Locate and identify every blood parasite.
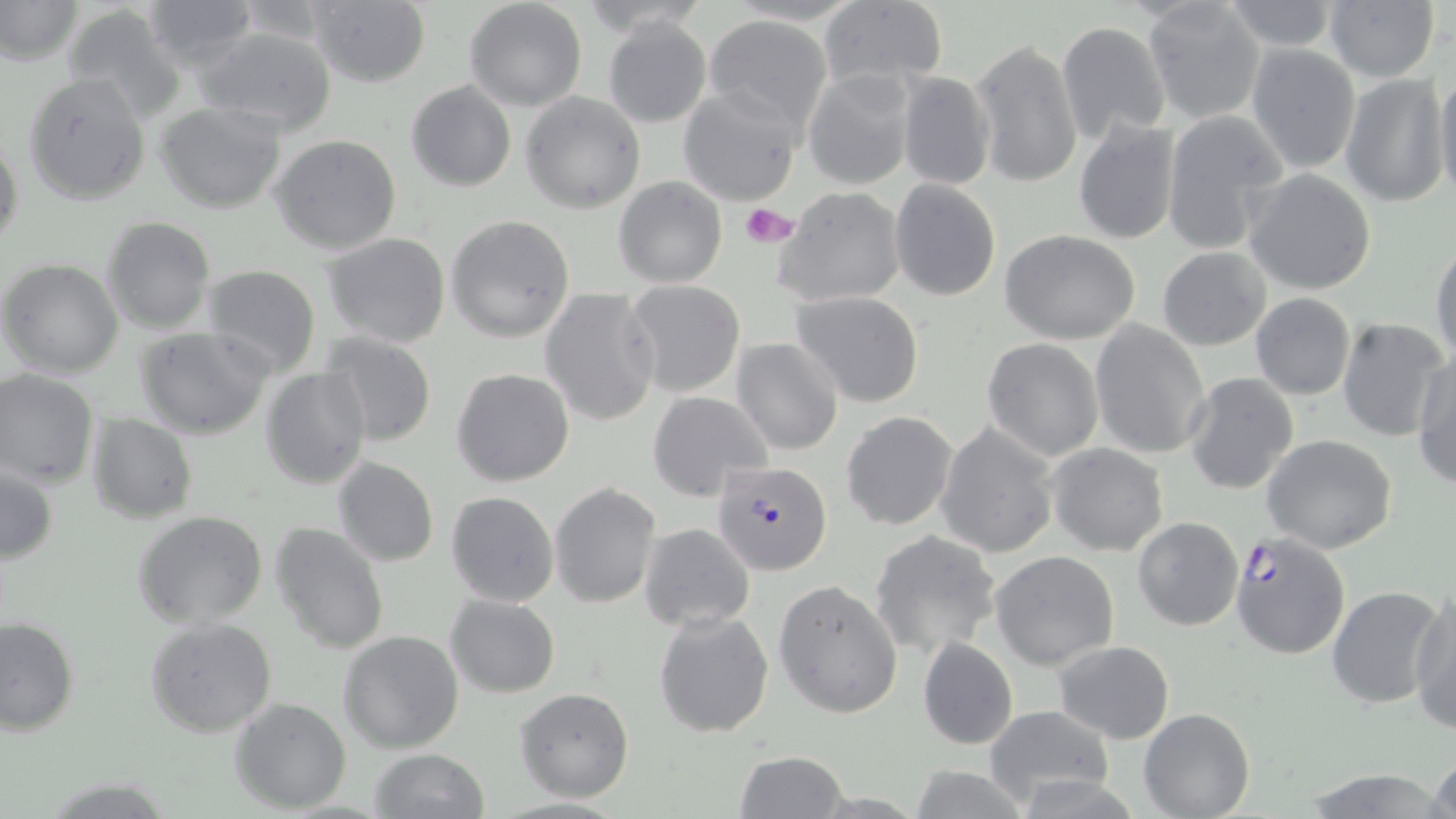
Approximate bounding boxes as [x1, y1, x2, y2] in pixels.
Plasmodium falciparum-infected red blood cells: [712, 458, 830, 573], [1228, 532, 1351, 659].
No Plasmodium ovale, Plasmodium malariae, Plasmodium vivax, Babesia divergens, or Trypanosoma brucei observed.

Uninfected red blood cell locations: [0, 0, 82, 66], [141, 0, 261, 71], [309, 0, 432, 88], [575, 0, 712, 33], [1221, 0, 1339, 52], [1321, 0, 1439, 83], [464, 1, 587, 111], [814, 2, 949, 92], [1143, 2, 1267, 123], [61, 4, 185, 122], [703, 14, 834, 136], [602, 16, 712, 129], [1057, 20, 1172, 144], [193, 26, 339, 135], [971, 37, 1083, 188], [1246, 43, 1360, 173], [1435, 68, 1456, 203], [801, 69, 919, 191], [897, 70, 996, 190], [23, 73, 152, 206], [1340, 74, 1448, 208], [405, 80, 516, 191], [677, 85, 803, 207], [520, 91, 646, 214], [153, 100, 288, 214], [1165, 109, 1291, 256], [1073, 117, 1182, 245], [0, 130, 24, 254], [271, 134, 403, 255], [1244, 168, 1377, 296], [614, 176, 727, 288], [889, 178, 1000, 301], [774, 185, 907, 307], [445, 215, 575, 342], [100, 216, 215, 333], [1002, 231, 1140, 345], [321, 233, 452, 349], [1431, 241, 1455, 368], [1158, 248, 1271, 350], [1, 258, 125, 380], [202, 265, 321, 379], [624, 280, 747, 399], [540, 288, 662, 427], [792, 291, 925, 408], [1249, 293, 1356, 399], [1337, 317, 1449, 442], [1088, 320, 1211, 460], [135, 327, 275, 440], [315, 333, 439, 447], [733, 337, 844, 455], [981, 338, 1105, 462], [1413, 351, 1456, 488], [261, 366, 370, 491], [451, 367, 575, 486], [0, 368, 99, 488], [1184, 372, 1300, 496], [647, 390, 773, 502], [840, 410, 957, 530], [86, 413, 197, 524], [935, 422, 1059, 559], [1264, 434, 1397, 553], [1048, 443, 1169, 556], [333, 457, 440, 568], [1, 465, 57, 564], [550, 482, 661, 608], [445, 491, 559, 607], [134, 510, 267, 629], [1132, 516, 1243, 632], [270, 521, 389, 654], [641, 523, 755, 631], [869, 530, 1001, 657], [989, 550, 1121, 670], [774, 580, 904, 717], [1326, 585, 1446, 708], [1409, 588, 1456, 734], [445, 594, 561, 697], [654, 609, 775, 738], [1, 616, 78, 736], [144, 617, 277, 737], [338, 629, 465, 754], [918, 637, 1019, 751], [1053, 640, 1176, 743], [515, 688, 634, 801], [229, 697, 351, 815], [983, 706, 1115, 809], [1139, 707, 1255, 819], [1426, 748, 1456, 819], [368, 749, 488, 819], [735, 749, 850, 818], [905, 765, 1032, 819], [1299, 769, 1445, 818], [1010, 775, 1145, 818]. Platelet locations: [740, 203, 799, 248]. Slide-level diagnosis: Plasmodium falciparum. May-Grünwald-Giemsa stain. 1000x magnification. Image is 1456×819 pixels. One field of a larger specimen. Thin blood smear. Optical microscopy.